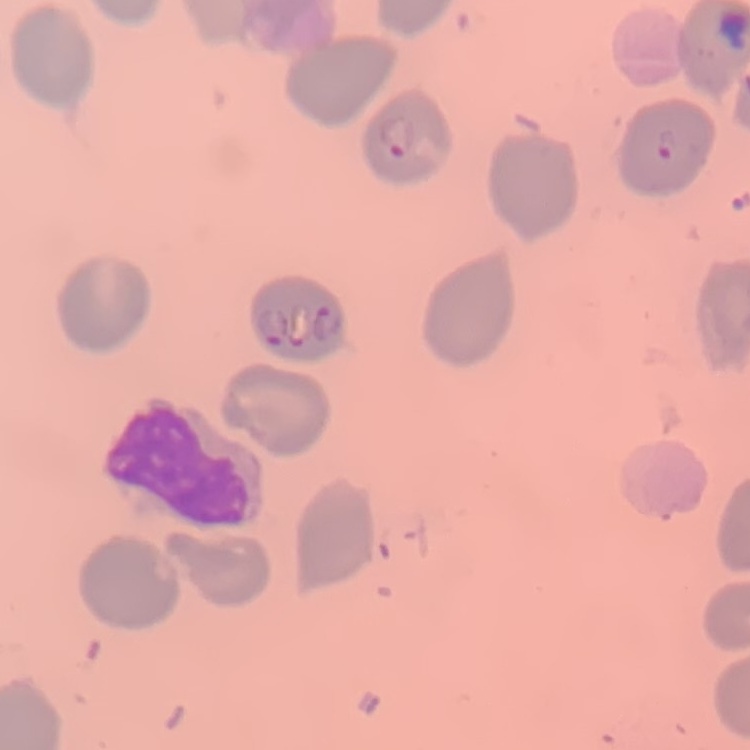

The red blood cells exhibit no rouleaux formation. Thin blood smear. Square crop of a larger photomicrograph. Field's or Giemsa stain.